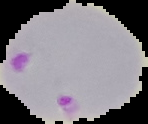

Summary:
  - Image type: segmented cell region on a black background
  - Preparation: thin blood film
  - Result: Plasmodium parasites detected
  - Image size: 148×124 pixels